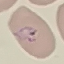 Malaria status: parasitized. Photographed with a smartphone camera at the microscope eyepiece. Cell patch, automatically extracted from a larger field of view and resized to 64 × 64 pixels. Giemsa-stained preparation. Thin blood film.